Assess this cell for malaria.
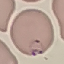

It is parasitized.

capture: smartphone through the microscope eyepiece
preparation: thin blood film
stain: Giemsa
image_type: cell patch, automatically extracted from a larger field of view and resized to 64 × 64 pixels